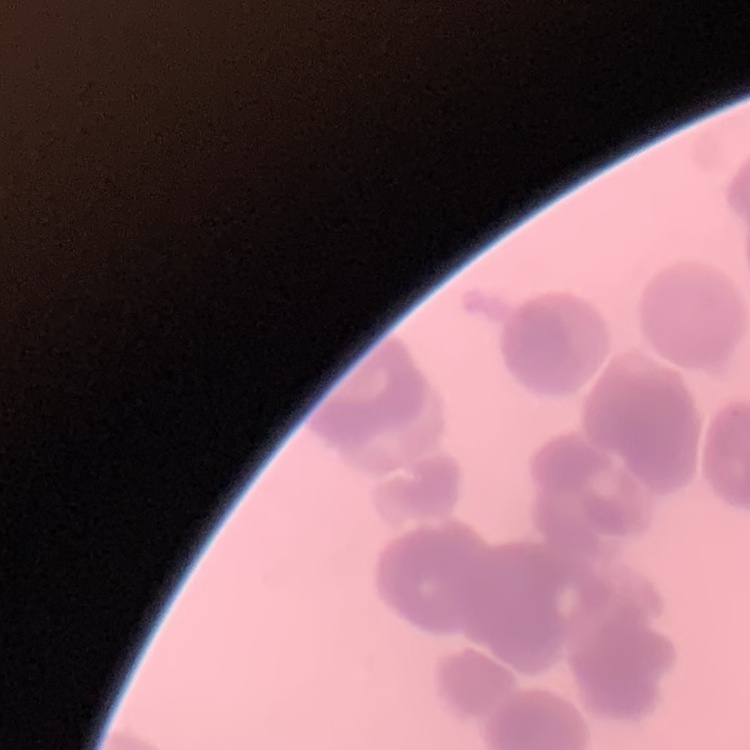

Summary:
  - Erythrocyte morphology: rouleaux formation
  - Preparation: thin blood film
  - Stain: Field's or Giemsa
  - Image type: one tile cut from a larger photomicrograph